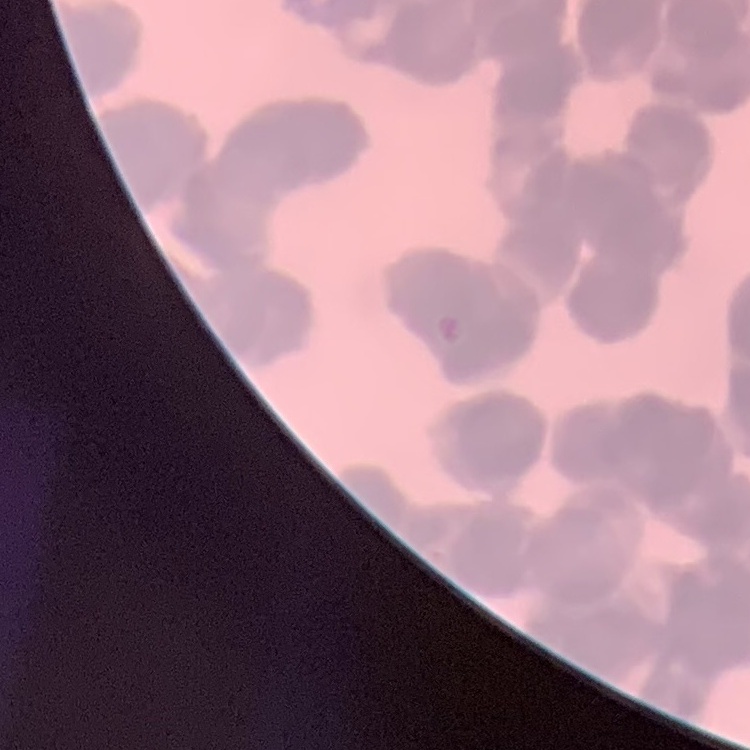
red blood cell morphology = rouleaux formation
preparation = thin peripheral smear
image type = one tile cut from a larger photomicrograph
stain = Field's or Giemsa